Classify this cell by malaria status.
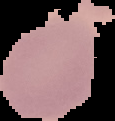
It is uninfected.

Summary:
  - Preparation: thin blood film
  - Image size: 115×121 pixels
  - Image type: cell region segmented out of the field of view; surrounding area masked to black